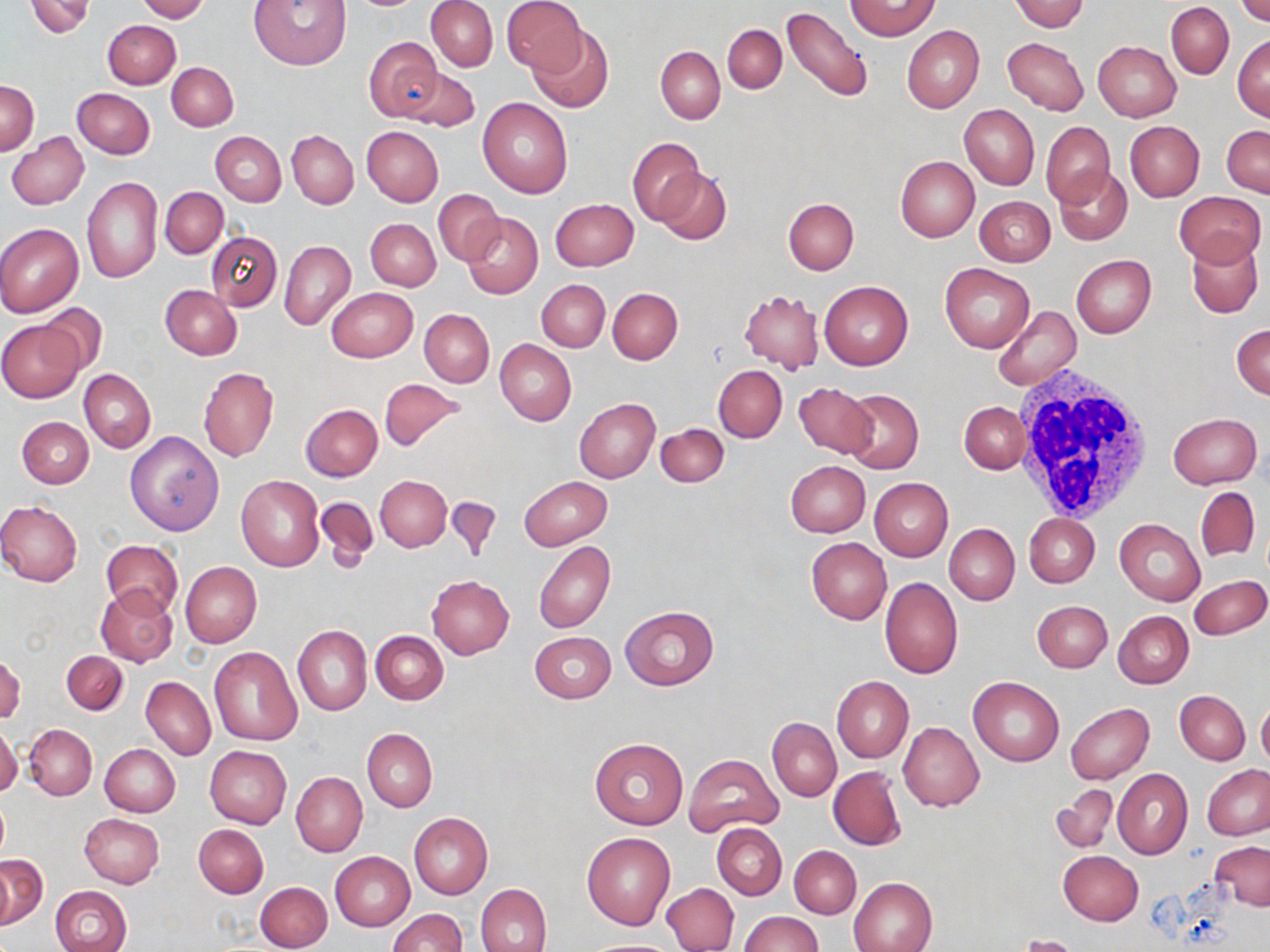
Summary:
  - Coordinate format: approximate bounding boxes as (x1, y1, x2, y2) in pixels
  - Uninfected red blood cell locations: (25, 0, 95, 38), (137, 0, 208, 21), (251, 0, 353, 70), (502, 0, 587, 76), (1011, 0, 1089, 33), (1234, 0, 1270, 26), (427, 1, 497, 71), (847, 2, 941, 40), (1166, 2, 1234, 78), (783, 5, 874, 103), (102, 20, 179, 89), (723, 24, 787, 93), (902, 25, 984, 113), (525, 26, 613, 115), (1233, 34, 1270, 121), (363, 37, 442, 120), (1001, 38, 1088, 116), (1093, 42, 1181, 122), (656, 46, 725, 123), (166, 62, 238, 131), (403, 67, 479, 131), (1, 82, 39, 154), (73, 88, 155, 158), (478, 98, 574, 198), (959, 104, 1039, 190), (1041, 121, 1115, 206), (1125, 121, 1204, 203), (1222, 124, 1270, 197), (361, 126, 443, 206), (7, 131, 89, 210), (287, 131, 358, 208), (211, 132, 286, 205), (627, 137, 705, 225), (895, 156, 980, 242), (655, 165, 731, 243), (1054, 167, 1132, 247), (82, 176, 162, 284), (161, 187, 228, 258), (434, 189, 504, 265), (1175, 189, 1265, 266), (975, 196, 1055, 267), (783, 197, 858, 274), (551, 199, 638, 271), (463, 213, 543, 298), (366, 219, 441, 291), (0, 223, 83, 317), (206, 232, 282, 311), (1187, 238, 1263, 318), (281, 241, 355, 330), (1071, 254, 1156, 338), (940, 264, 1034, 352), (537, 279, 609, 352), (819, 279, 914, 370), (160, 284, 241, 360), (326, 287, 418, 362), (607, 287, 683, 364), (740, 289, 824, 374), (35, 304, 108, 379), (993, 305, 1082, 390), (419, 309, 494, 387), (1, 320, 83, 402), (1232, 322, 1270, 399), (495, 340, 575, 426), (713, 365, 787, 442), (198, 367, 279, 461), (79, 370, 156, 452), (378, 377, 467, 451), (795, 382, 877, 458), (842, 389, 924, 472), (573, 398, 659, 483), (959, 401, 1030, 473), (300, 403, 383, 481), (1167, 411, 1262, 489), (17, 416, 94, 488), (657, 423, 729, 487), (125, 430, 225, 535), (785, 461, 870, 537), (236, 475, 324, 572), (376, 476, 451, 551), (520, 476, 612, 549), (869, 477, 953, 561), (1196, 487, 1259, 562), (445, 496, 503, 564), (315, 497, 379, 572), (0, 500, 84, 586), (1024, 513, 1099, 588), (1115, 519, 1206, 605), (943, 524, 1019, 606), (805, 537, 892, 625), (101, 538, 182, 619), (535, 542, 615, 633), (180, 561, 261, 648), (1188, 574, 1269, 641), (427, 575, 515, 659), (879, 576, 963, 679), (96, 585, 178, 667), (1032, 600, 1112, 672), (620, 605, 719, 690), (1113, 610, 1194, 689), (292, 625, 371, 715), (529, 629, 616, 703), (370, 631, 448, 704), (209, 646, 301, 746), (61, 651, 128, 714), (1, 652, 25, 724), (831, 676, 913, 762), (141, 677, 216, 760), (968, 677, 1063, 765), (1175, 690, 1250, 764), (1257, 698, 1270, 772), (1066, 702, 1154, 784), (768, 717, 841, 800), (898, 721, 984, 812), (0, 722, 21, 799), (24, 724, 97, 800), (362, 729, 437, 811), (590, 739, 686, 829), (99, 744, 179, 817), (205, 746, 291, 828), (683, 753, 784, 837), (1202, 764, 1270, 841), (828, 766, 906, 851), (1113, 769, 1193, 859), (291, 771, 367, 856), (1052, 784, 1118, 853), (409, 812, 492, 899), (79, 814, 164, 888), (194, 823, 268, 898), (713, 824, 787, 899), (582, 832, 676, 930), (1210, 841, 1270, 910), (790, 846, 861, 918), (1057, 850, 1143, 925), (330, 851, 414, 931), (1, 855, 47, 929), (849, 877, 937, 952), (256, 882, 331, 951), (477, 883, 551, 952), (662, 883, 738, 951), (50, 885, 132, 952), (388, 909, 466, 952), (740, 912, 822, 952), (1017, 935, 1081, 952), (583, 938, 679, 951)
  - White blood cell locations: (1012, 366, 1156, 521)
  - Slide-level diagnosis: no evidence of blood parasites
  - Field of view: single
  - Modality: optical microscopy
  - Magnification: 1000x
  - Stain: May-Grünwald-Giemsa
  - Preparation: thin blood smear
  - Image size: 1270×952 pixels